Comment on the morphology of the erythrocytes.
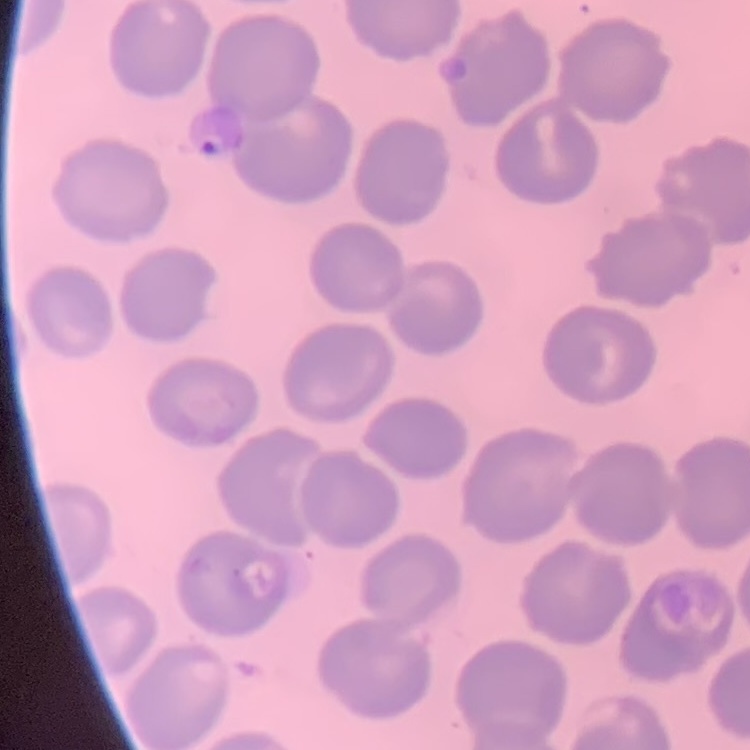
They show no rouleaux formation.

Thin peripheral smear. Stained with either Field's or Giemsa. Square crop of a larger photomicrograph.